Give the position of every Plasmodium parasite.
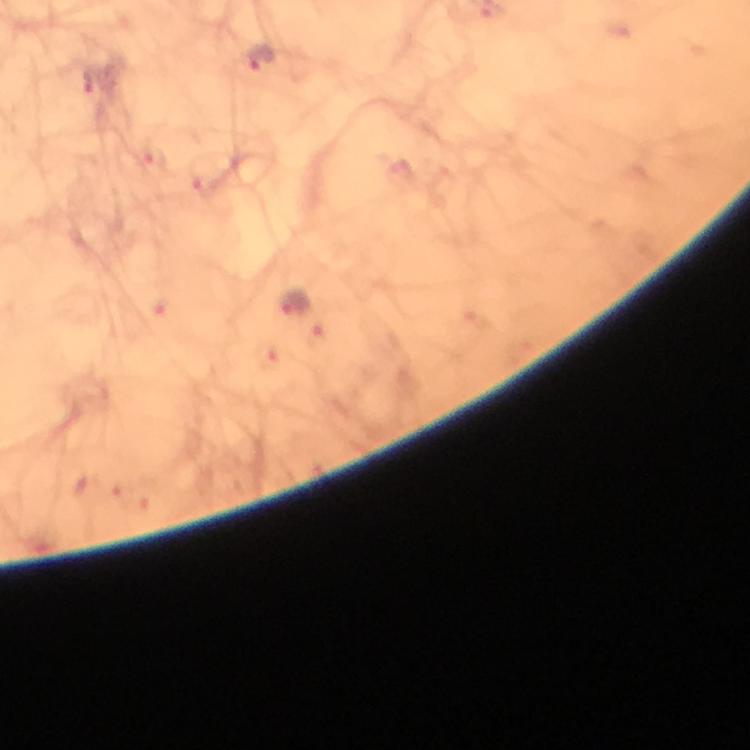

Approximate centers as [x, y] in pixels.
Plasmodium parasites: [259, 58], [293, 304].

Immersion oil was used. At 100x magnification. Photographed with a smartphone mounted on the microscope. A crop from one field of view. Image is 750×750 pixels. Thick blood smear. From a malaria diagnostic workup. Giemsa-stained preparation.